Comment on the morphology of the red blood cells.
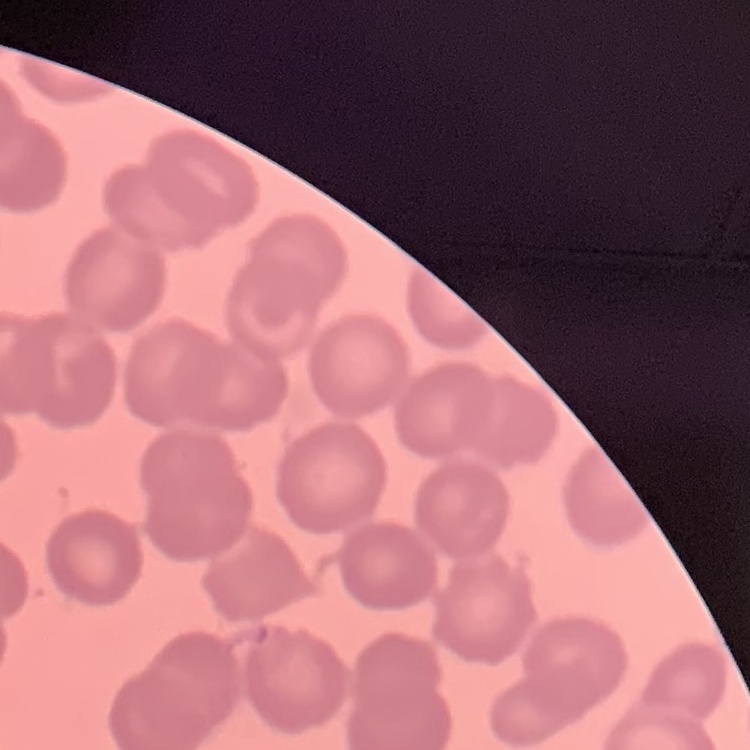

No rouleaux formation.

Summary:
  - Preparation: thin blood film
  - Image type: square crop of a larger photomicrograph
  - Stain: Field's or Giemsa